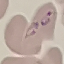 Result: malaria parasites identified. Automatically extracted cell patch, resized to 64 × 64 pixels. Acquired by smartphone through the microscope eyepiece. Thin blood smear. Giemsa-stained preparation.